Assess for malaria.
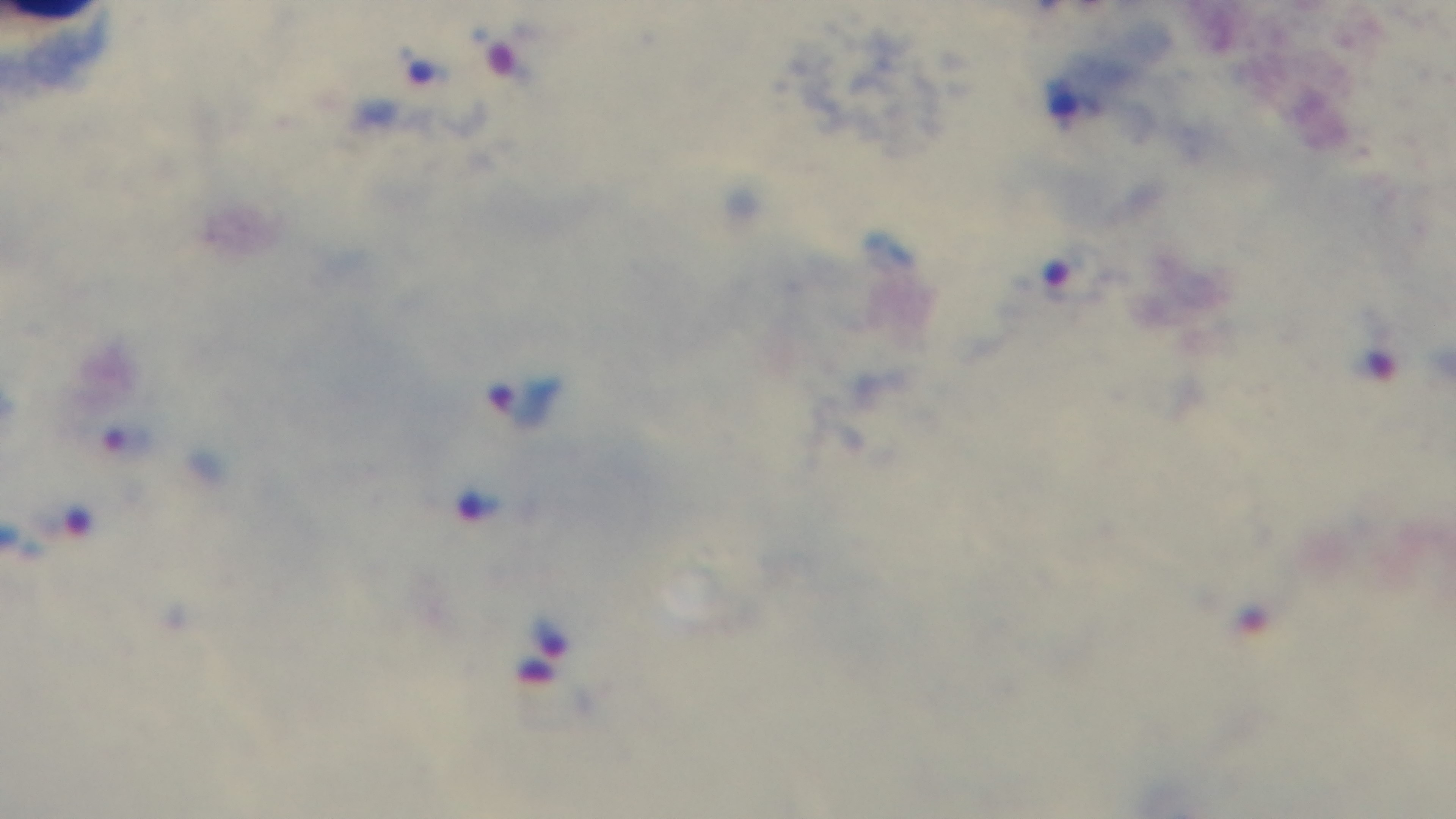
Infected.

Summary:
  - Preparation: thick blood film
  - Field of view: single
  - Capture: mounted 4K digital camera
  - Modality: light microscopy
  - Stain: Giemsa
  - Objective: 100x oil immersion